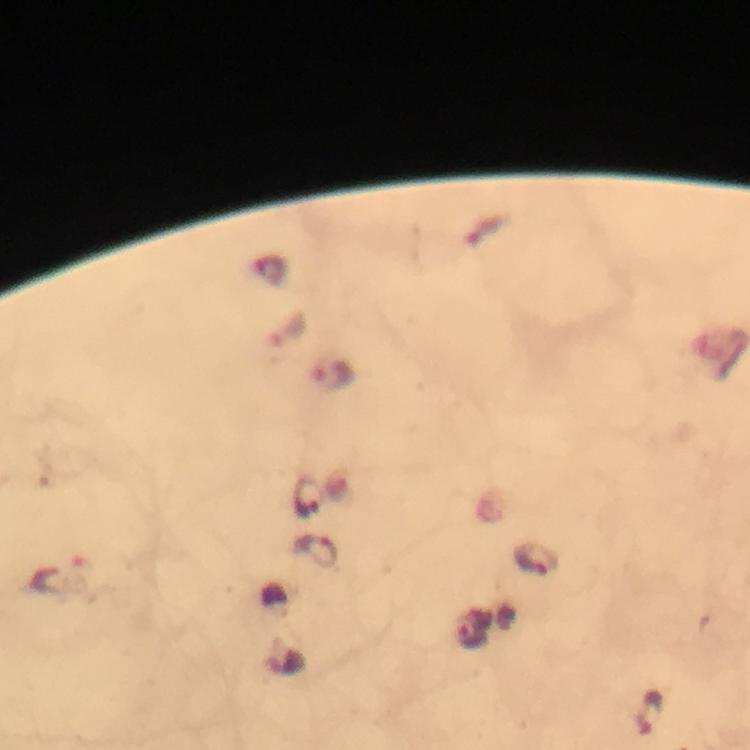
Approximate centers as (x, y) in pixels.
Summary:
  - Malaria parasite locations: (288, 331), (335, 375), (307, 498), (315, 551), (538, 560), (59, 571), (473, 632), (649, 712)
  - Context: from a malaria diagnostic workup
  - Image size: 750×750 pixels
  - Capture: smartphone camera through the microscope
  - Stain: Giemsa
  - Cropped from: a single field of view
  - Immersion oil: used
  - Magnification: 100x
  - Preparation: thick blood smear